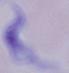
Summary:
  - Magnification: 1000x
  - Identification: trypanosome
  - Modality: micrograph